Classify this cell by malaria status.
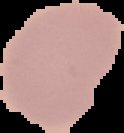

Uninfected.

preparation: thin blood smear
image_type: segmented cell region with the area outside set to black
image_size: 124×133 pixels